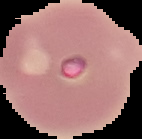

Summary:
  - Image type: segmented cell region on a black background
  - Preparation: thin blood smear
  - Malaria status: uninfected
  - Image size: 142×139 pixels